Identify the blood parasite species.
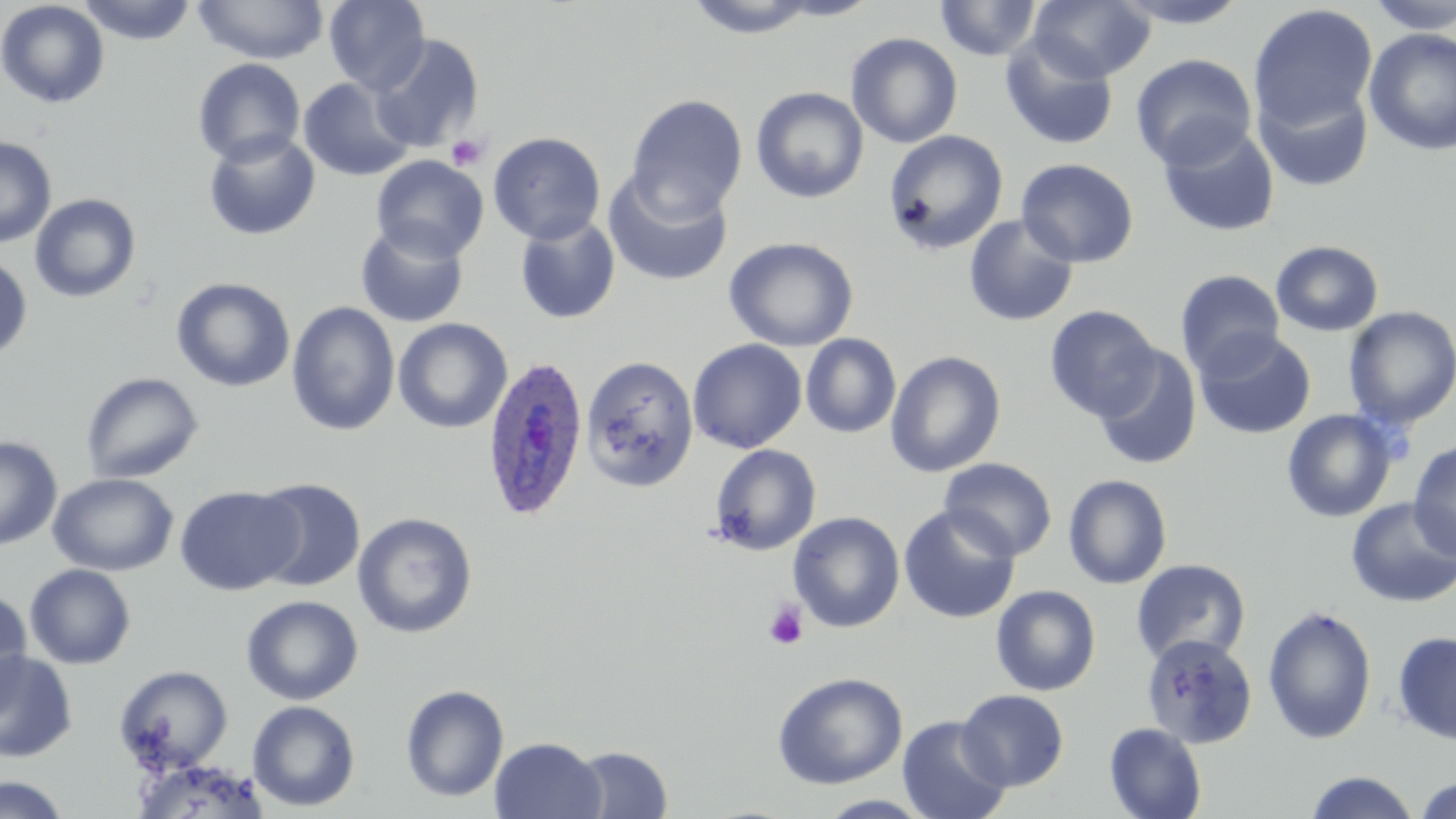
Plasmodium ovale.

Summary:
  - Coordinate format: approximate bounding boxes as [x1, y1, x2, y2] in pixels
  - Plasmodium ovale-infected red blood cell locations (subset): [482, 354, 589, 521]
  - Uninfected red blood cell locations (subset): [78, 0, 198, 45], [194, 0, 328, 65], [323, 0, 431, 94], [684, 0, 823, 39], [767, 0, 884, 20], [934, 0, 1042, 61], [1028, 0, 1155, 83], [1109, 0, 1253, 28], [1366, 0, 1456, 35], [0, 1, 109, 109], [1248, 4, 1378, 130], [1363, 28, 1456, 155], [845, 32, 963, 148], [370, 34, 484, 153], [1000, 34, 1119, 151], [1130, 53, 1257, 170], [192, 58, 306, 166], [298, 78, 416, 182], [1255, 81, 1374, 192], [750, 87, 869, 203], [625, 94, 748, 221], [1158, 123, 1280, 237], [203, 130, 321, 241], [883, 130, 1008, 256], [488, 131, 606, 245], [0, 136, 57, 248], [371, 155, 489, 263], [1016, 159, 1139, 268], [602, 171, 733, 288], [29, 193, 142, 303], [963, 214, 1079, 327], [514, 215, 621, 325], [355, 221, 469, 328], [724, 236, 858, 352], [1271, 240, 1383, 336], [0, 253, 33, 362], [1175, 269, 1286, 378], [171, 277, 295, 392], [286, 301, 400, 436], [1044, 305, 1161, 421], [1343, 306, 1456, 428], [393, 318, 512, 433], [1193, 329, 1316, 440], [800, 333, 901, 438], [687, 339, 807, 454], [1092, 346, 1202, 470], [885, 351, 1006, 477], [581, 355, 699, 491], [80, 371, 204, 485], [1281, 408, 1399, 523], [0, 436, 62, 550], [1408, 441, 1456, 560], [709, 444, 822, 555], [939, 457, 1057, 561], [48, 472, 179, 576], [1063, 474, 1172, 590], [251, 478, 366, 592], [174, 485, 303, 596], [1345, 497, 1456, 608], [898, 505, 1020, 625], [352, 512, 478, 638], [788, 512, 905, 633], [1130, 559, 1251, 667], [24, 564, 136, 669], [990, 585, 1101, 696], [0, 587, 33, 718], [240, 595, 364, 705], [1262, 605, 1377, 744], [1392, 631, 1456, 745], [0, 651, 78, 763], [114, 664, 233, 773], [771, 671, 908, 790], [400, 684, 509, 802], [956, 689, 1069, 791], [247, 700, 360, 812], [897, 714, 1011, 819], [1104, 722, 1207, 819], [489, 736, 607, 819], [569, 745, 673, 819], [129, 756, 269, 819], [1305, 771, 1421, 819], [0, 774, 72, 818], [1414, 776, 1456, 819], [814, 794, 935, 819]
  - Platelet locations: [445, 133, 490, 171], [764, 601, 808, 650]
  - Field of view: single
  - Image size: 1456×819 pixels
  - Magnification: 1000x
  - Modality: light microscopy
  - Preparation: thin blood smear
  - Stain: May-Grünwald-Giemsa